Point out each leukocyte.
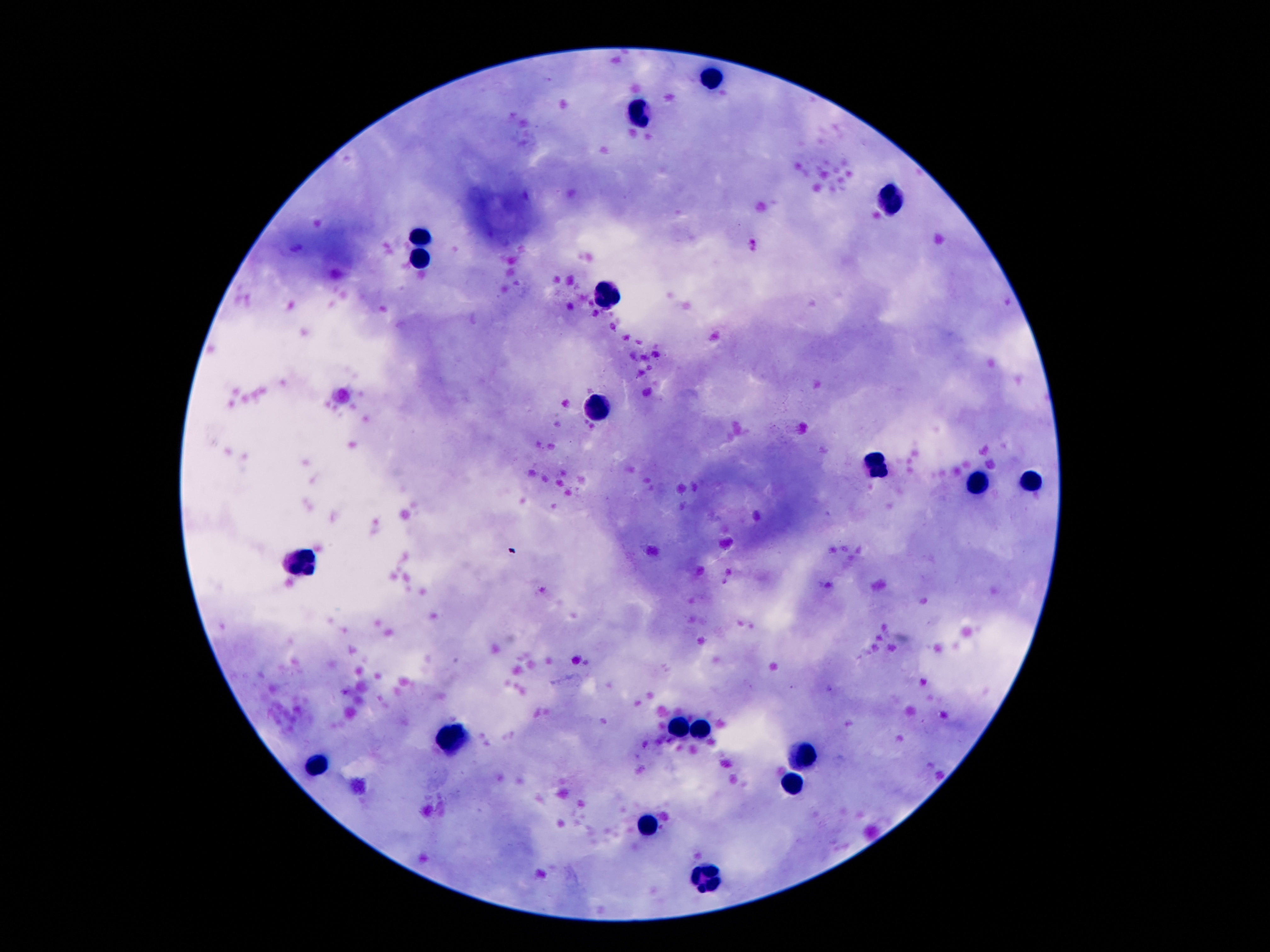
Approximate centers as {x, y} in pixels.
Leukocytes: {713, 76}, {640, 115}, {890, 199}, {420, 235}, {420, 262}, {611, 297}, {597, 412}, {877, 467}, {1029, 483}, {976, 484}, {302, 564}, {677, 731}, {699, 735}, {452, 742}, {799, 757}, {318, 764}, {788, 781}, {647, 825}, {704, 878}.

Summary:
  - Preparation: thick blood film
  - Capture: smartphone camera through the microscope eyepiece
  - Magnification: 100x
  - Stain: Giemsa
  - Image size: 1270×952 pixels
  - Patient malaria status: not infected
  - Field of view: one from this slide